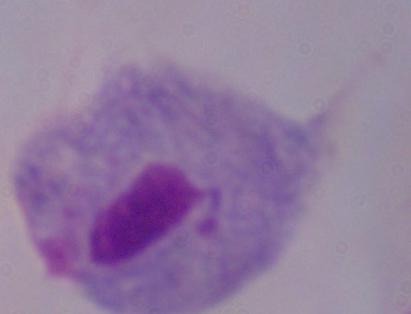
Photomicrograph. A trichomonad is seen. Captured at 1000x magnification.